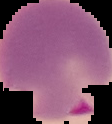
Malaria status: parasitized. Image is 112×124 pixels. Cell region segmented out of the field of view; the surrounding area is masked to black. From a thin blood smear.